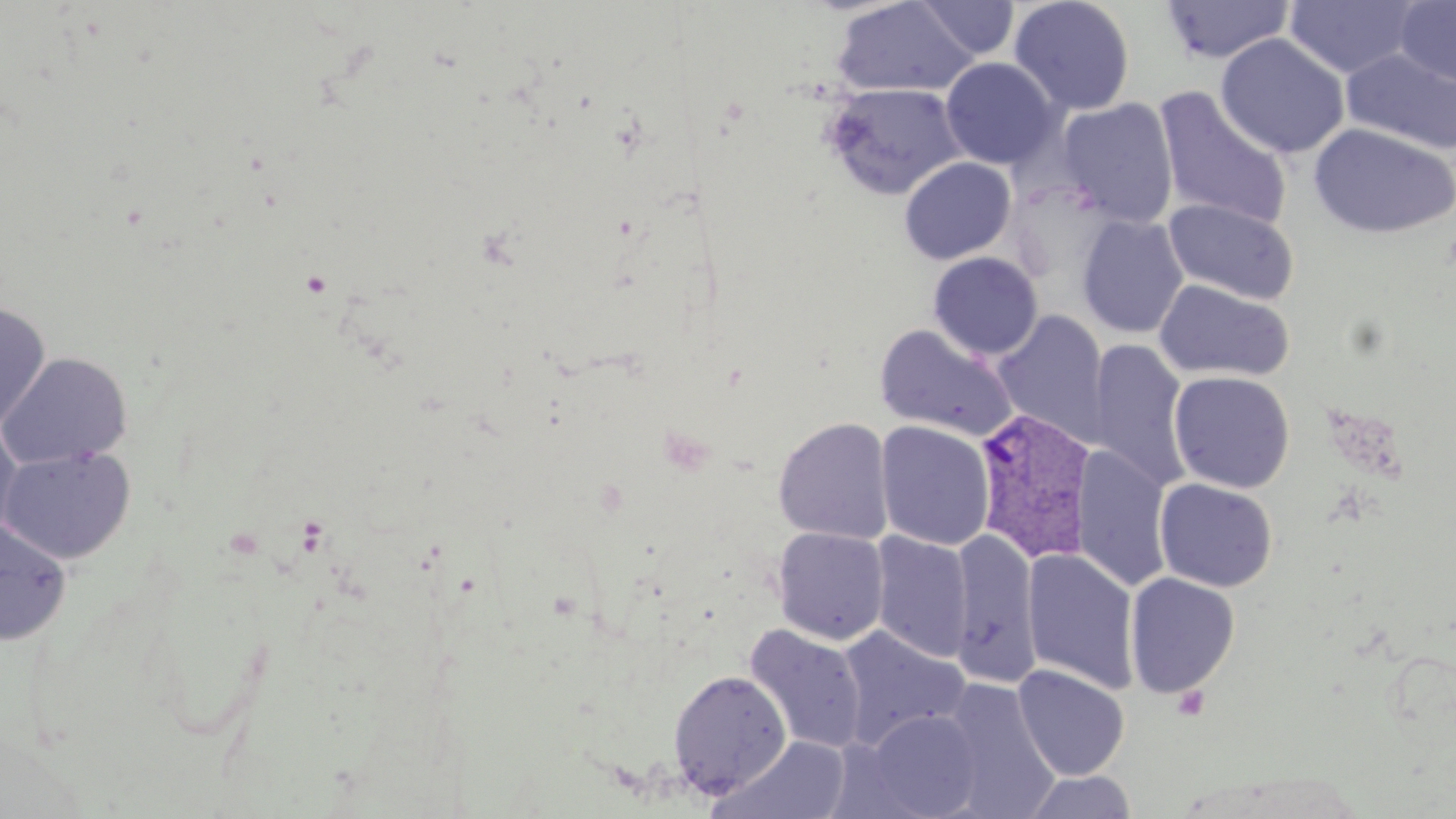

slide-level diagnosis = Plasmodium vivax
modality = light microscopy
Plasmodium vivax-infected red blood cell locations = approximate bounding boxes as [x1, y1, x2, y2] in pixels: [972, 407, 1098, 566]
uninfected red blood cell locations = approximate bounding boxes as [x1, y1, x2, y2] in pixels: [832, 0, 980, 98], [1009, 0, 1135, 116], [914, 1, 1020, 59], [1160, 1, 1296, 63], [1284, 1, 1424, 78], [1395, 1, 1456, 88], [1216, 33, 1350, 159], [1341, 46, 1456, 156], [940, 57, 1062, 170], [822, 82, 967, 200], [1154, 88, 1292, 231], [1057, 97, 1178, 228], [1309, 123, 1455, 239], [899, 157, 1016, 264], [1164, 198, 1299, 306], [1077, 215, 1189, 338], [928, 252, 1043, 360], [1154, 281, 1295, 383], [0, 302, 51, 432], [992, 310, 1110, 448], [875, 325, 1019, 443], [1089, 339, 1192, 491], [0, 351, 133, 469], [1169, 370, 1295, 493], [773, 417, 893, 544], [875, 420, 995, 550], [0, 421, 23, 544], [0, 444, 137, 564], [1071, 446, 1173, 592], [1154, 477, 1278, 592], [0, 516, 72, 646], [772, 528, 889, 645], [951, 530, 1040, 685], [870, 531, 973, 663], [1022, 549, 1141, 695], [1124, 572, 1240, 699], [744, 624, 868, 754], [835, 625, 971, 752], [1012, 664, 1129, 780], [668, 669, 792, 798], [939, 679, 1060, 818], [861, 709, 983, 818], [710, 736, 855, 819], [1022, 770, 1139, 818]
field of view = one of a larger specimen
preparation = thin blood smear
stain = May-Grünwald-Giemsa
image size = 1456×819 pixels
magnification = 1000x